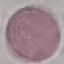
Summary:
  - Malaria status: uninfected
  - Preparation: thin blood film
  - Capture: smartphone through the microscope eyepiece
  - Image type: cell patch, automatically extracted from a larger field of view and resized to 64 × 64 pixels
  - Stain: Giemsa